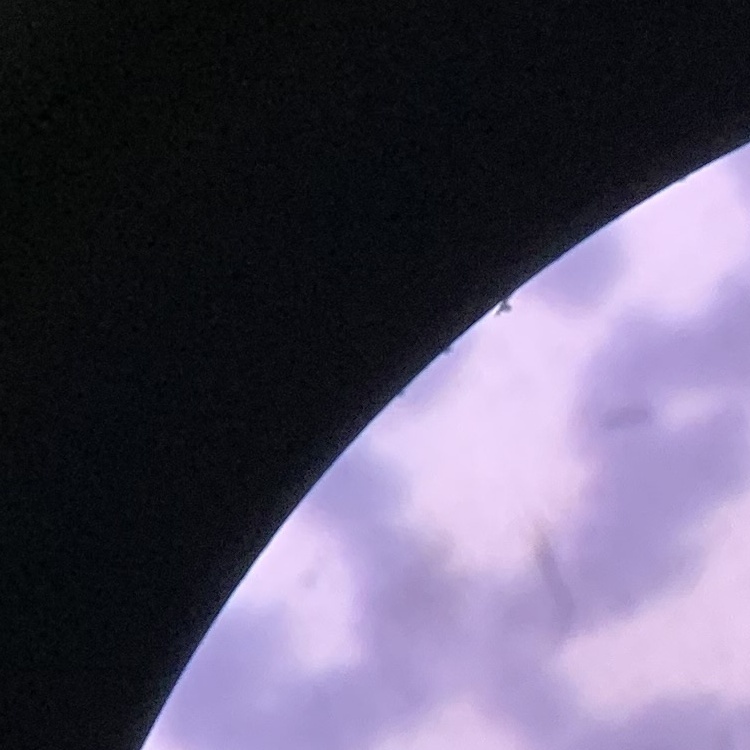
Summary:
  - Red blood cell morphology: rouleaux formation
  - Stain: Field's or Giemsa
  - Preparation: thin blood film
  - Image type: square crop of a larger photomicrograph